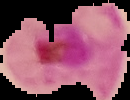
From a thin blood smear. Image is 130×100 pixels. Cell region segmented out of the field of view; the surrounding area is masked to black. Result: Plasmodium parasites identified.